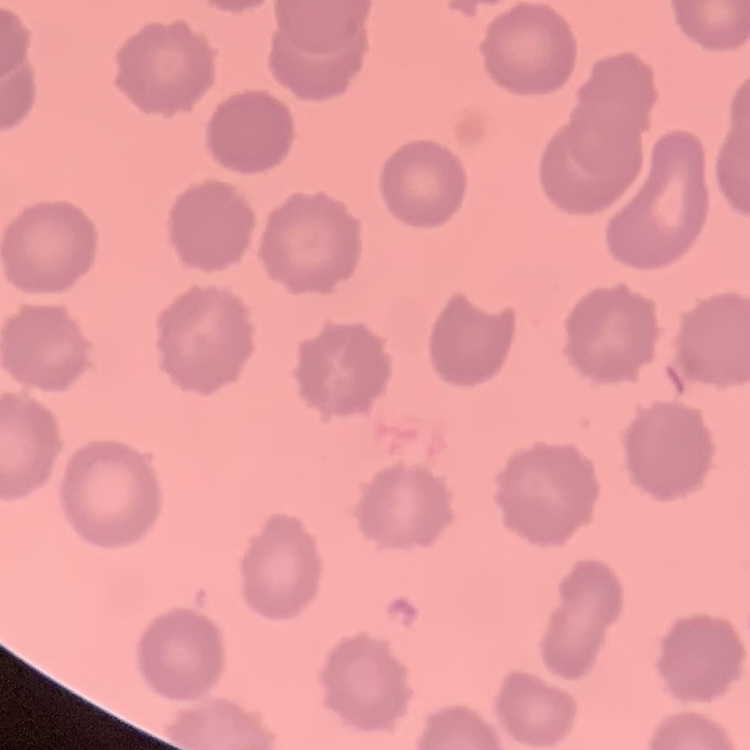
Summary:
  - Erythrocyte morphology: no rouleaux formation
  - Stain: Field's or Giemsa
  - Preparation: thin blood film
  - Image type: one tile cut from a larger photomicrograph